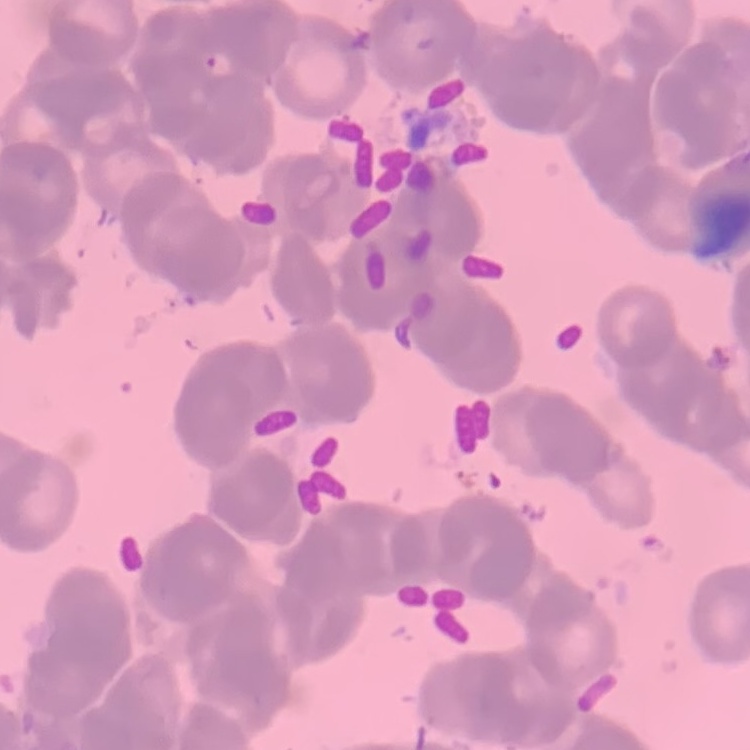
red blood cell morphology = rouleaux formation
image type = one tile cut from a larger photomicrograph
preparation = thin peripheral smear
stain = Field's or Giemsa